Classify this cell by malaria status.
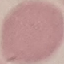
It is uninfected.

stain: Giemsa
preparation: thin smear
image_type: cell patch, automatically extracted from a larger field of view and resized to 64 × 64 pixels
capture: smartphone camera at the microscope eyepiece